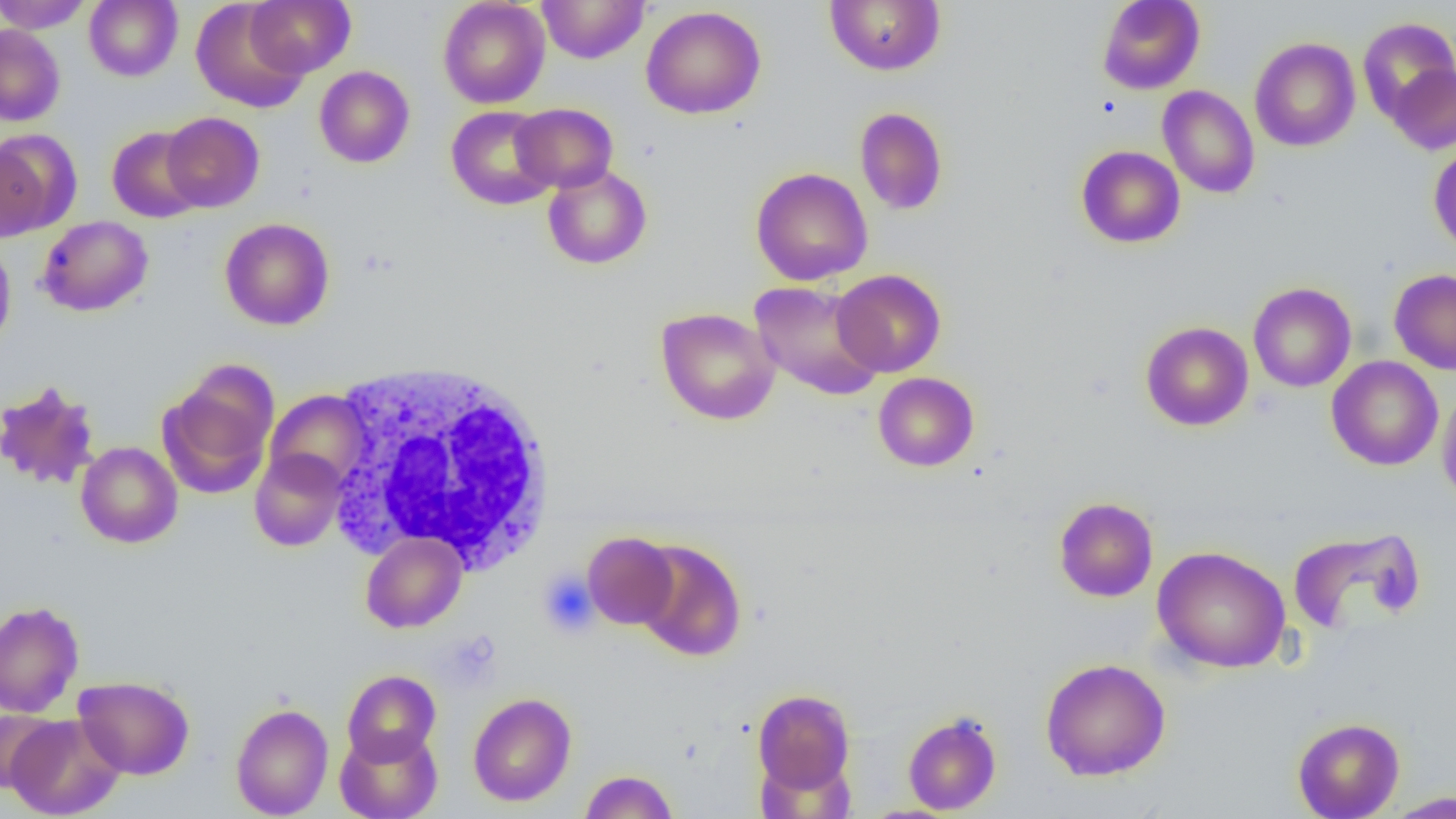 Approximate bounding boxes as named x1/y1/x2/y2 corners in pixels. White blood cell locations: (x1=328, y1=359, x2=559, y2=575). Platelet locations: (x1=538, y1=569, x2=598, y2=637). Uninfected red blood cell locations: (x1=0, y1=0, x2=92, y2=33), (x1=84, y1=0, x2=183, y2=82), (x1=245, y1=0, x2=355, y2=77), (x1=438, y1=0, x2=550, y2=109), (x1=537, y1=0, x2=650, y2=64), (x1=825, y1=0, x2=945, y2=75), (x1=1097, y1=0, x2=1205, y2=95), (x1=191, y1=1, x2=309, y2=113), (x1=641, y1=5, x2=766, y2=119), (x1=1357, y1=17, x2=1456, y2=122), (x1=0, y1=24, x2=65, y2=126), (x1=1250, y1=37, x2=1361, y2=152), (x1=1388, y1=63, x2=1456, y2=154), (x1=314, y1=66, x2=414, y2=168), (x1=1157, y1=85, x2=1260, y2=199), (x1=511, y1=103, x2=618, y2=193), (x1=446, y1=106, x2=557, y2=210), (x1=855, y1=107, x2=948, y2=216), (x1=161, y1=112, x2=265, y2=212), (x1=107, y1=126, x2=206, y2=223), (x1=2, y1=130, x2=79, y2=235), (x1=1428, y1=142, x2=1456, y2=255), (x1=1076, y1=145, x2=1185, y2=248), (x1=542, y1=164, x2=652, y2=270), (x1=750, y1=167, x2=873, y2=286), (x1=36, y1=216, x2=153, y2=317), (x1=220, y1=218, x2=335, y2=330), (x1=0, y1=240, x2=16, y2=353), (x1=832, y1=269, x2=946, y2=377), (x1=1389, y1=269, x2=1456, y2=375), (x1=749, y1=280, x2=885, y2=401), (x1=1248, y1=282, x2=1357, y2=392), (x1=656, y1=307, x2=780, y2=425), (x1=1140, y1=321, x2=1254, y2=431), (x1=1326, y1=356, x2=1443, y2=471), (x1=158, y1=365, x2=278, y2=499), (x1=873, y1=372, x2=979, y2=472), (x1=0, y1=380, x2=101, y2=491), (x1=1437, y1=385, x2=1456, y2=509), (x1=264, y1=389, x2=372, y2=492), (x1=76, y1=441, x2=182, y2=548), (x1=250, y1=449, x2=347, y2=551), (x1=1053, y1=496, x2=1158, y2=602), (x1=360, y1=531, x2=467, y2=633), (x1=583, y1=531, x2=678, y2=629), (x1=1289, y1=531, x2=1428, y2=640), (x1=634, y1=539, x2=747, y2=661), (x1=1152, y1=545, x2=1291, y2=673), (x1=0, y1=601, x2=84, y2=717), (x1=1040, y1=657, x2=1171, y2=781), (x1=342, y1=669, x2=441, y2=765), (x1=73, y1=675, x2=194, y2=780), (x1=752, y1=689, x2=855, y2=793), (x1=468, y1=692, x2=577, y2=807), (x1=230, y1=703, x2=334, y2=818), (x1=0, y1=709, x2=62, y2=793), (x1=902, y1=711, x2=1002, y2=815), (x1=5, y1=714, x2=125, y2=818), (x1=1292, y1=717, x2=1404, y2=819), (x1=334, y1=727, x2=443, y2=819), (x1=579, y1=769, x2=679, y2=818), (x1=1384, y1=791, x2=1456, y2=818). Slide-level diagnosis: negative for blood parasites. Optical microscopy. Image is 1456×819 pixels. 1000x magnification. Thin blood smear. Single field of view.